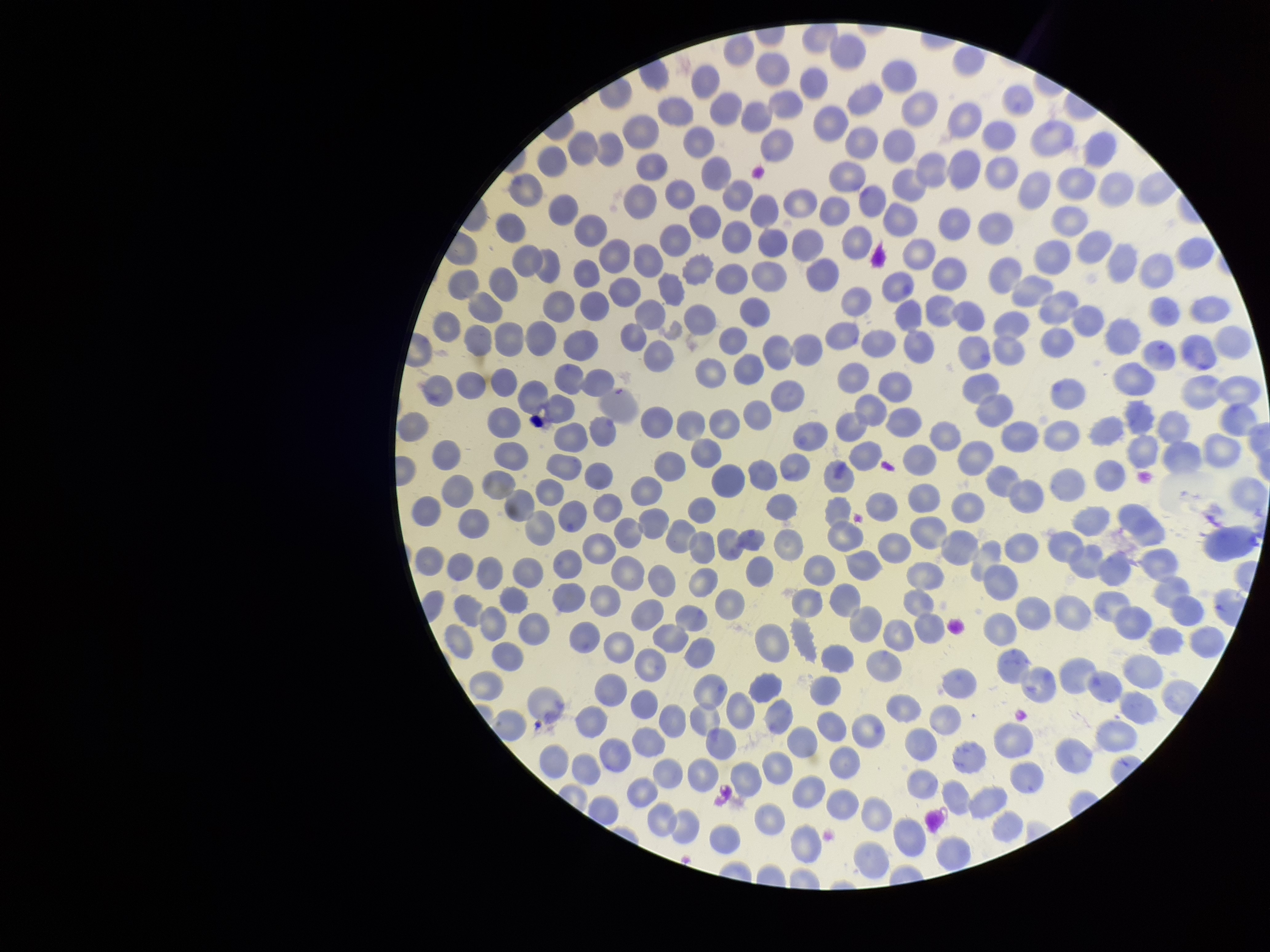

Summary:
  - Field of view: one from this slide
  - Stain: Giemsa
  - Red blood cell count: 323
  - Parasitized red blood cells: none seen
  - Preparation: thin
  - Patient malaria status: negative
  - Capture: smartphone photograph through the microscope eyepiece
  - Image size: 1270×952 pixels
  - Parasitized red blood cell count: 0